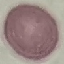

Result: no malaria parasites seen. Giemsa-stained preparation. Acquired by smartphone through the microscope eyepiece. Thin blood smear. Automatically extracted cell patch, resized to 64 × 64 pixels.